State which cell type is depicted.
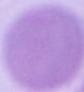

This is an erythrocyte.

Micrograph. 1000x magnification.